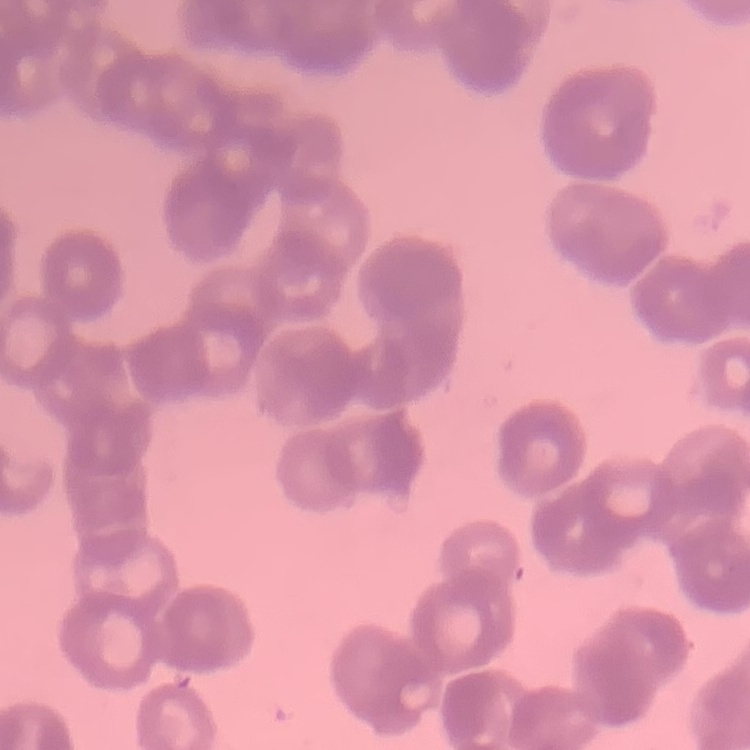

Summary:
  - Red blood cell morphology: rouleaux formation
  - Preparation: thin peripheral smear
  - Stain: Field's or Giemsa
  - Image type: square crop of a larger photomicrograph